Outline each blood parasite and name the species.
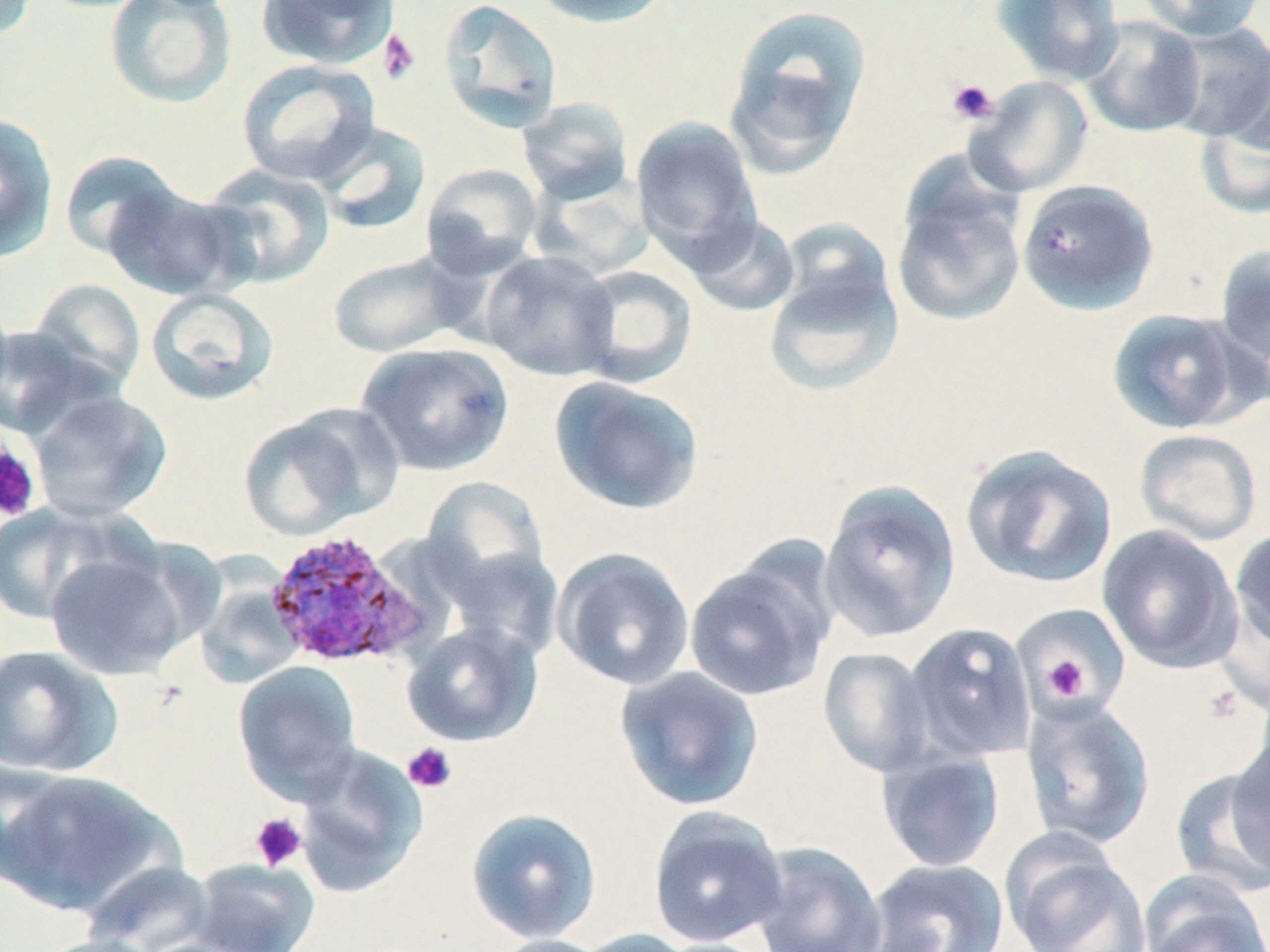

Approximate bounding boxes as (x1, y1, x2, y2) in pixels.
Plasmodium ovale-infected red blood cells: (263, 527, 432, 670).
No Plasmodium falciparum, Plasmodium malariae, Plasmodium vivax, Babesia divergens, or Trypanosoma brucei observed.

{
  "slide_level_diagnosis": "Plasmodium ovale",
  "field_of_view": "one of a larger specimen",
  "preparation": "thin blood smear",
  "magnification": "1000x",
  "stain": "May-Grünwald-Giemsa",
  "uninfected_red_blood_cell_locations": "approximate bounding boxes as (x1, y1, x2, y2) in pixels: (0, 0, 38, 42), (103, 0, 238, 110), (255, 0, 400, 71), (438, 0, 563, 133), (529, 0, 674, 28), (990, 0, 1125, 85), (1136, 0, 1267, 41), (724, 5, 872, 176), (1080, 15, 1206, 138), (1165, 23, 1270, 142), (236, 59, 380, 186), (965, 76, 1093, 197), (517, 97, 634, 205), (1195, 100, 1270, 220), (0, 114, 59, 263), (631, 117, 762, 264), (313, 120, 432, 237), (58, 149, 184, 262), (421, 162, 543, 277), (198, 164, 336, 290), (530, 168, 655, 280), (892, 177, 1026, 328), (1016, 179, 1159, 315), (102, 182, 245, 301), (683, 211, 802, 318), (762, 228, 905, 398), (1214, 242, 1270, 378), (480, 249, 620, 381), (326, 250, 476, 359), (572, 265, 697, 388), (27, 279, 146, 397), (145, 287, 280, 406), (1106, 308, 1254, 435), (0, 324, 103, 441), (356, 341, 515, 477), (549, 376, 705, 516), (29, 390, 172, 522), (238, 406, 393, 540), (1134, 428, 1263, 546), (960, 444, 1119, 589), (420, 477, 552, 604), (818, 479, 962, 644), (0, 503, 126, 626), (1097, 524, 1243, 675), (1229, 526, 1270, 657), (435, 527, 561, 659), (46, 544, 196, 682), (552, 547, 696, 691), (683, 548, 838, 702), (192, 570, 305, 689), (1017, 612, 1129, 712), (401, 621, 543, 747), (902, 622, 1037, 764), (0, 645, 124, 778), (817, 647, 938, 778), (232, 661, 363, 802), (615, 667, 765, 812), (1020, 696, 1156, 850), (1226, 731, 1270, 876), (293, 744, 428, 901), (876, 746, 1006, 872), (0, 759, 75, 889), (1170, 766, 1270, 899), (0, 769, 178, 917), (647, 806, 789, 948), (465, 807, 603, 943), (1003, 839, 1151, 952), (749, 841, 888, 952), (188, 858, 321, 952), (863, 858, 1009, 952), (81, 861, 218, 952), (1139, 872, 1269, 952), (570, 929, 702, 952), (32, 934, 167, 952), (487, 935, 613, 952)",
  "image_size": "1270×952 pixels",
  "modality": "light microscopy",
  "platelet_locations": "approximate bounding boxes as (x1, y1, x2, y2) in pixels: (377, 29, 421, 85), (946, 78, 999, 125), (0, 437, 42, 523), (1042, 655, 1092, 700), (1202, 684, 1247, 726), (402, 742, 457, 794), (249, 812, 308, 871)"
}